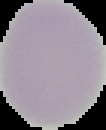

Summary:
  - Preparation: thin blood smear
  - Image type: segmented cell region with the area outside set to black
  - Malaria status: uninfected
  - Image size: 106×130 pixels